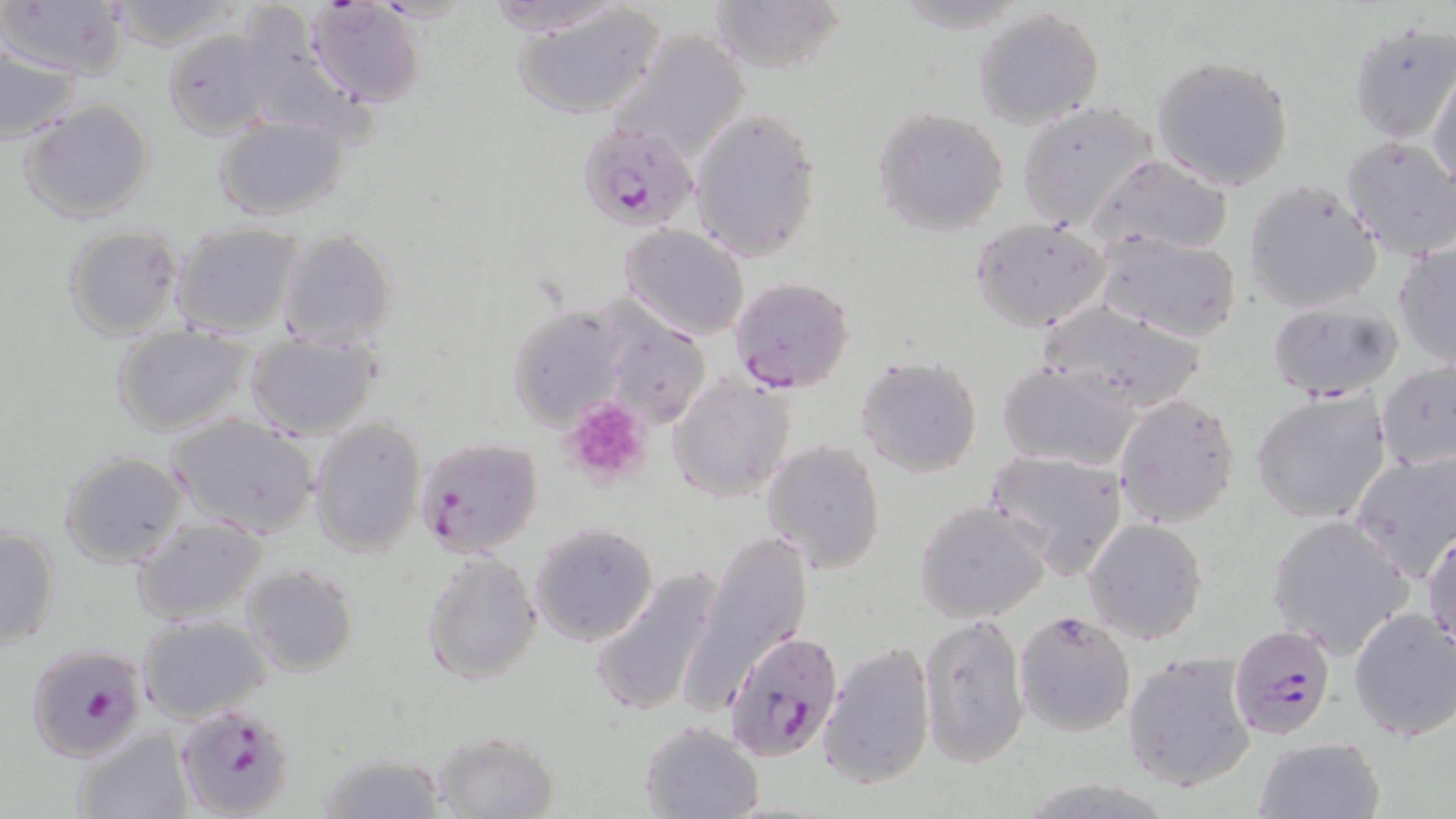 Approximate bounding boxes as (x1,y1)-(x2,y2) corner pairs in pixels. Plasmodium falciparum-infected red blood cell locations: (577,123)-(700,232), (727,276)-(855,393), (413,436)-(545,558), (1228,623)-(1336,738), (722,629)-(845,762), (25,642)-(149,761), (175,702)-(296,818). Uninfected red blood cell locations: (305,0)-(425,109), (479,0)-(634,37), (510,0)-(667,120), (707,0)-(846,72), (3,1)-(130,80), (104,1)-(241,50), (973,8)-(1104,130), (1348,20)-(1456,144), (162,28)-(273,139), (606,29)-(750,166), (0,46)-(84,145), (1151,53)-(1295,191), (1428,64)-(1456,193), (20,97)-(154,223), (1016,102)-(1158,228), (689,104)-(821,263), (871,106)-(1010,235), (211,113)-(350,221), (1339,136)-(1456,261), (1090,154)-(1234,257), (1243,180)-(1384,313), (970,217)-(1112,332), (171,221)-(305,338), (617,222)-(750,340), (62,224)-(183,340), (277,228)-(397,348), (1096,231)-(1244,342), (1392,240)-(1456,369), (1266,297)-(1402,400), (507,304)-(631,430), (1038,304)-(1209,412), (602,310)-(713,429), (111,327)-(254,436), (243,331)-(384,441), (855,354)-(983,478), (996,361)-(1142,471), (1376,362)-(1456,472), (668,371)-(797,502), (1250,389)-(1391,526), (1114,393)-(1241,528), (167,414)-(319,537), (309,416)-(427,558), (762,439)-(885,572), (985,448)-(1131,578), (1347,449)-(1456,584), (58,451)-(187,569), (914,500)-(1053,624), (1268,513)-(1413,659), (132,517)-(269,626), (1084,518)-(1208,644), (529,522)-(658,646), (1,523)-(61,652), (1425,529)-(1456,655), (692,530)-(815,700), (422,551)-(542,683), (587,563)-(728,721), (242,564)-(358,676), (1348,606)-(1456,743), (1014,608)-(1136,739), (918,611)-(1030,770), (136,614)-(270,722), (817,640)-(937,791), (1122,651)-(1256,792), (639,720)-(766,818), (71,727)-(192,819), (429,729)-(559,818), (1253,736)-(1385,819), (318,751)-(448,819). Platelet locations: (561,398)-(653,490). Slide-level diagnosis: Plasmodium falciparum. May-Grünwald-Giemsa-stained preparation. Thin blood smear. Single field of view. Image is 1456×819 pixels. 1000x magnification. Optical microscopy.